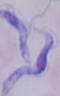 Photomicrograph. 1000x magnification. A trypanosome is shown.